Report the malaria status of this cell.
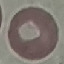
Uninfected.

stain = Giemsa
image type = cell patch, automatically extracted from a larger field of view and resized to 64 × 64 pixels
capture = smartphone through the microscope eyepiece
preparation = thin blood smear